Name the blood parasite species.
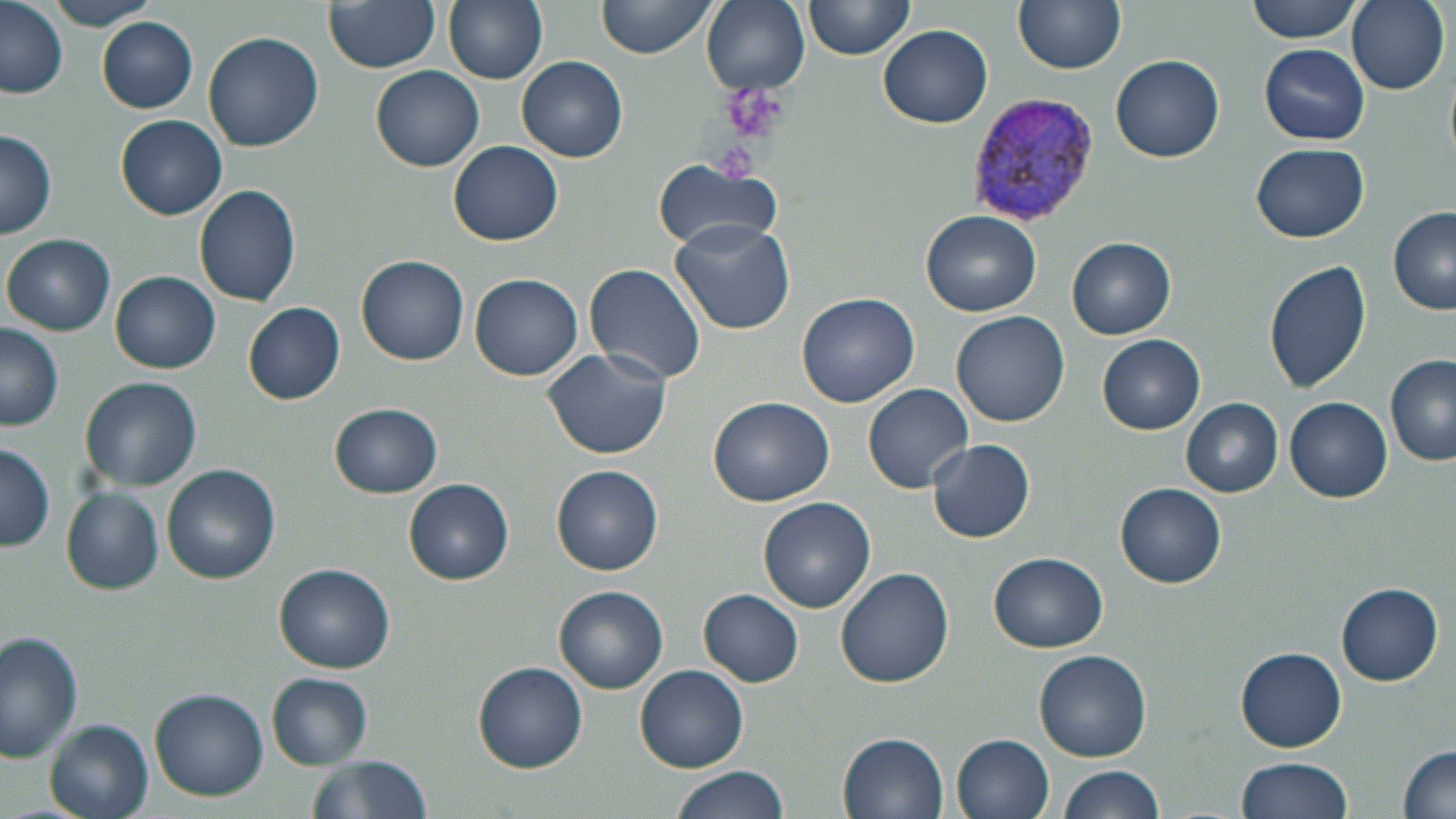
Plasmodium vivax.

field of view = single
magnification = 1000x
modality = light microscopy
Plasmodium vivax-infected red blood cell locations = approximate bounding boxes as (x1, y1, x2, y2) in pixels: (965, 92, 1101, 226)
stain = May-Grünwald-Giemsa
image size = 1456×819 pixels
platelet locations = approximate bounding boxes as (x1, y1, x2, y2) in pixels: (723, 83, 788, 144), (714, 146, 760, 186)
uninfected red blood cell locations = approximate bounding boxes as (x1, y1, x2, y2) in pixels: (324, 0, 440, 73), (444, 0, 548, 84), (597, 0, 719, 59), (701, 0, 809, 93), (803, 0, 915, 60), (1013, 0, 1126, 74), (1246, 0, 1364, 42), (1347, 0, 1449, 93), (43, 1, 163, 30), (0, 2, 70, 100), (98, 19, 198, 112), (879, 25, 993, 127), (202, 31, 323, 151), (1258, 43, 1369, 145), (1111, 54, 1225, 163), (518, 56, 628, 162), (371, 65, 485, 172), (117, 114, 227, 219), (0, 129, 59, 238), (449, 140, 563, 245), (1251, 144, 1370, 242), (652, 161, 782, 252), (193, 184, 301, 308), (1388, 206, 1456, 313), (921, 210, 1042, 316), (669, 220, 796, 334), (3, 234, 115, 336), (1067, 237, 1175, 339), (357, 255, 468, 364), (1261, 256, 1372, 395), (585, 263, 706, 386), (111, 271, 220, 374), (469, 273, 583, 381), (798, 292, 921, 407), (243, 301, 347, 403), (952, 310, 1069, 426), (0, 323, 64, 432), (1099, 334, 1205, 434), (542, 349, 672, 459), (1386, 354, 1456, 466), (80, 376, 202, 492), (863, 383, 973, 493), (709, 396, 834, 507), (1285, 397, 1392, 502), (1180, 398, 1282, 497), (331, 404, 442, 497), (928, 438, 1036, 543), (0, 441, 54, 554), (163, 463, 280, 584), (553, 465, 663, 577), (406, 480, 513, 583), (1117, 482, 1226, 586), (62, 489, 163, 594), (759, 497, 876, 613), (990, 551, 1108, 651), (275, 564, 395, 673), (836, 567, 954, 687), (1335, 583, 1444, 685), (555, 587, 667, 691), (699, 588, 803, 686), (0, 630, 82, 765), (1033, 649, 1152, 762), (1236, 649, 1346, 751), (475, 661, 587, 772), (636, 665, 748, 772), (266, 674, 372, 768), (150, 688, 269, 801), (45, 719, 154, 819), (839, 732, 948, 817), (952, 733, 1055, 818), (1396, 744, 1456, 818), (304, 755, 435, 819), (1236, 756, 1355, 818), (1054, 765, 1164, 819), (669, 767, 789, 819)
preparation = thin blood film